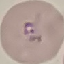
Summary:
  - Result: malaria parasites identified
  - Stain: Giemsa
  - Image type: automatically extracted cell patch, resized to 64 × 64 pixels
  - Preparation: thin smear
  - Capture: smartphone camera at the microscope eyepiece